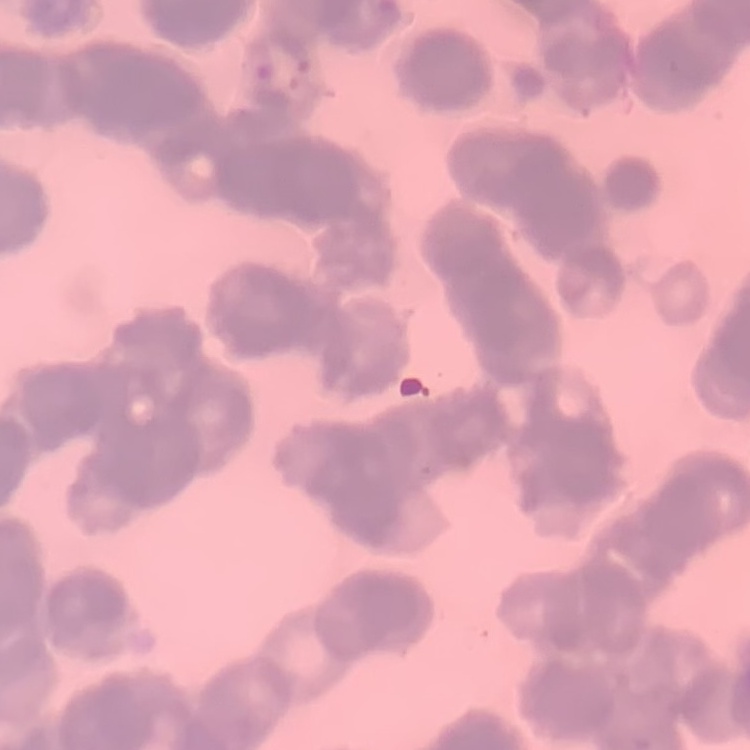
The erythrocytes exhibit rouleaux formation. Square crop of a larger photomicrograph. Stained with either Field's or Giemsa. Thin peripheral smear.